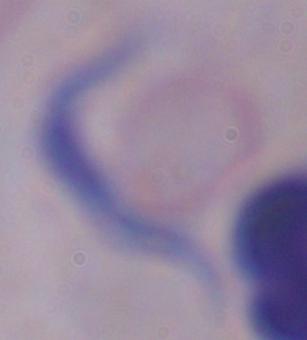

Captured at 1000x magnification. Photomicrograph. A trypanosome is shown.